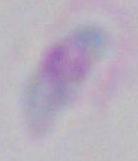
Toxoplasma gondii is seen. 1000x magnification. Photomicrograph.